Give the preparation type.
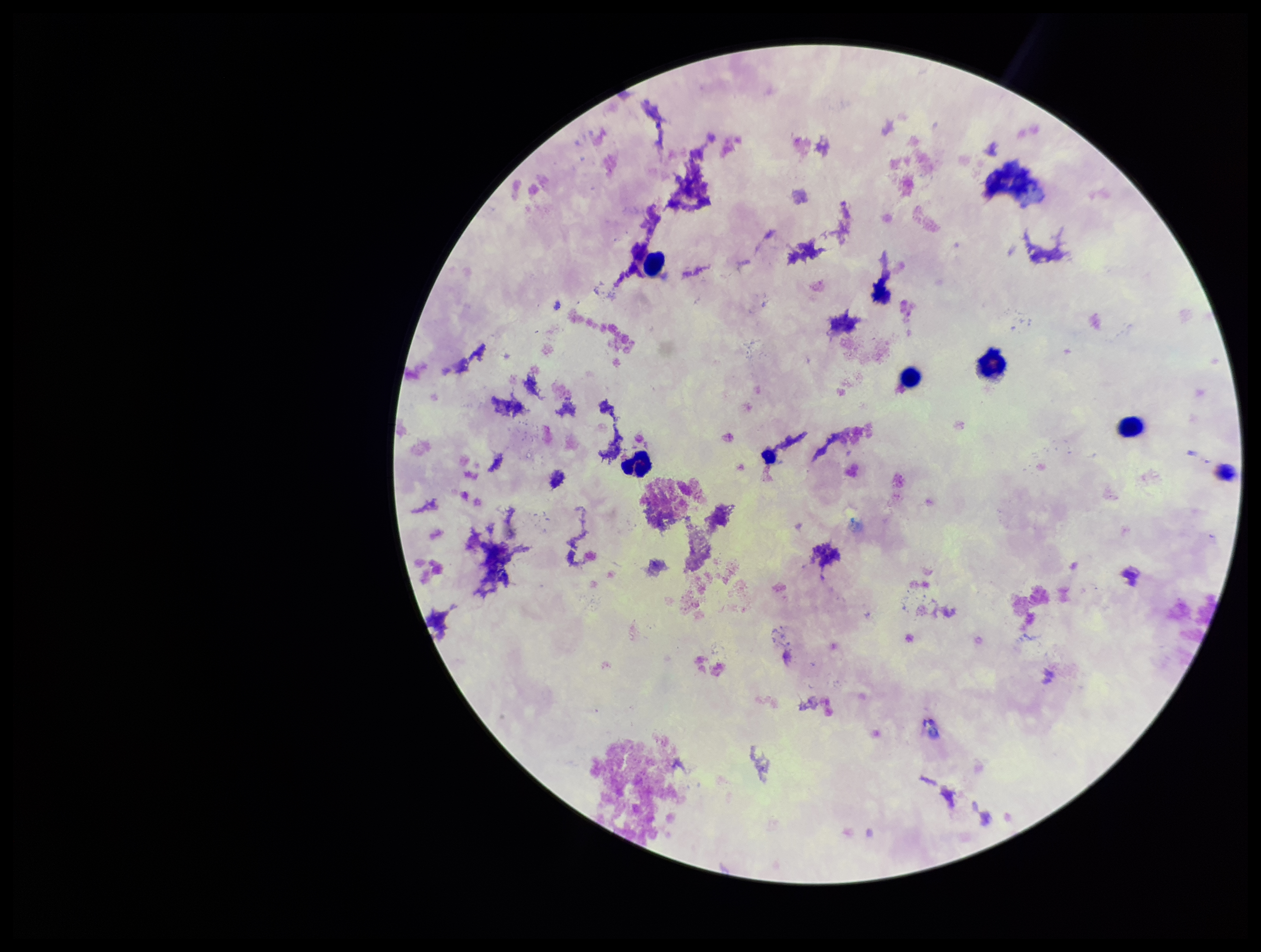

It is a thick blood smear.

Summary:
  - Patient malaria status: negative
  - Leukocyte count: 5
  - Capture: smartphone photograph through the microscope eyepiece
  - Field of view: single
  - Image size: 1261×952 pixels
  - Plasmodium parasites: none seen
  - Parasite count: 0
  - Stain: Giemsa